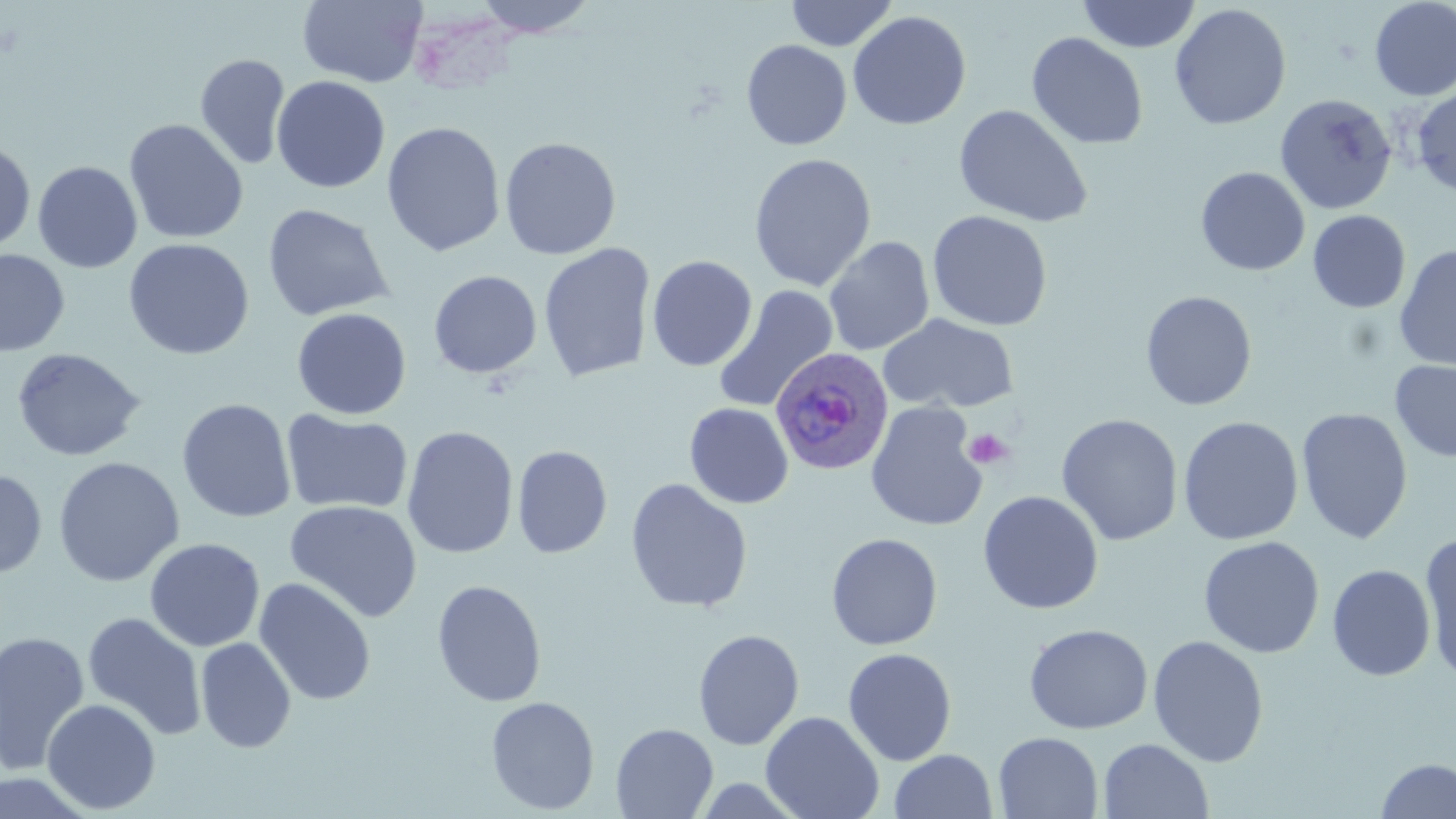

{
  "plasmodium_ovale_infected_red_blood_cell_locations": "approximate bounding boxes as named x1/y1/x2/y2 corners in pixels: (x1=770, y1=348, x2=892, y2=475)",
  "slide_level_diagnosis": "Plasmodium ovale",
  "platelet_locations": "approximate bounding boxes as named x1/y1/x2/y2 corners in pixels: (x1=964, y1=427, x2=1014, y2=471)",
  "image_size": "1456×819 pixels",
  "magnification": "1000x",
  "uninfected_red_blood_cell_locations": "approximate bounding boxes as named x1/y1/x2/y2 corners in pixels: (x1=297, y1=0, x2=427, y2=87), (x1=470, y1=0, x2=603, y2=38), (x1=785, y1=0, x2=898, y2=51), (x1=1077, y1=0, x2=1201, y2=53), (x1=1369, y1=1, x2=1456, y2=101), (x1=1170, y1=3, x2=1291, y2=131), (x1=847, y1=10, x2=971, y2=130), (x1=1026, y1=32, x2=1148, y2=149), (x1=741, y1=40, x2=852, y2=150), (x1=195, y1=53, x2=291, y2=170), (x1=271, y1=75, x2=391, y2=193), (x1=1411, y1=85, x2=1456, y2=197), (x1=1275, y1=93, x2=1397, y2=215), (x1=953, y1=105, x2=1093, y2=228), (x1=123, y1=119, x2=249, y2=245), (x1=382, y1=121, x2=506, y2=256), (x1=499, y1=136, x2=621, y2=260), (x1=0, y1=138, x2=36, y2=253), (x1=748, y1=152, x2=877, y2=292), (x1=32, y1=161, x2=143, y2=273), (x1=1195, y1=167, x2=1311, y2=276), (x1=261, y1=203, x2=393, y2=322), (x1=927, y1=210, x2=1053, y2=331), (x1=1307, y1=210, x2=1411, y2=313), (x1=823, y1=236, x2=934, y2=356), (x1=123, y1=238, x2=254, y2=360), (x1=538, y1=243, x2=656, y2=383), (x1=1394, y1=244, x2=1456, y2=372), (x1=0, y1=249, x2=70, y2=357), (x1=647, y1=255, x2=757, y2=372), (x1=428, y1=270, x2=542, y2=378), (x1=713, y1=285, x2=838, y2=413), (x1=1140, y1=290, x2=1257, y2=411), (x1=291, y1=308, x2=411, y2=419), (x1=878, y1=313, x2=1019, y2=414), (x1=12, y1=347, x2=146, y2=463), (x1=1390, y1=359, x2=1456, y2=463), (x1=177, y1=397, x2=296, y2=524), (x1=865, y1=402, x2=988, y2=532), (x1=684, y1=403, x2=794, y2=509), (x1=1296, y1=408, x2=1413, y2=544), (x1=281, y1=409, x2=413, y2=516), (x1=1057, y1=414, x2=1183, y2=546), (x1=1178, y1=416, x2=1303, y2=545), (x1=401, y1=425, x2=519, y2=560), (x1=512, y1=445, x2=613, y2=559), (x1=53, y1=456, x2=185, y2=587), (x1=0, y1=469, x2=47, y2=579), (x1=625, y1=478, x2=753, y2=613), (x1=977, y1=491, x2=1103, y2=614), (x1=284, y1=499, x2=422, y2=623), (x1=826, y1=532, x2=943, y2=651), (x1=1419, y1=533, x2=1456, y2=682), (x1=1198, y1=536, x2=1324, y2=658), (x1=144, y1=537, x2=265, y2=652), (x1=1327, y1=564, x2=1435, y2=681), (x1=253, y1=578, x2=377, y2=706), (x1=431, y1=579, x2=547, y2=707), (x1=82, y1=612, x2=207, y2=741), (x1=1023, y1=623, x2=1154, y2=734), (x1=693, y1=628, x2=804, y2=750), (x1=0, y1=630, x2=91, y2=776), (x1=1147, y1=635, x2=1269, y2=767), (x1=195, y1=637, x2=296, y2=753), (x1=842, y1=647, x2=957, y2=766), (x1=485, y1=696, x2=600, y2=815), (x1=42, y1=698, x2=161, y2=814), (x1=760, y1=711, x2=884, y2=819), (x1=610, y1=723, x2=719, y2=818), (x1=993, y1=732, x2=1103, y2=818), (x1=1098, y1=738, x2=1214, y2=819), (x1=889, y1=749, x2=998, y2=819), (x1=1375, y1=758, x2=1456, y2=818)",
  "stain": "May-Grünwald-Giemsa",
  "field_of_view": "single",
  "modality": "light microscopy",
  "preparation": "thin blood film"
}